Name the parasite shown.
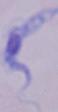

This is a trypanosome.

magnification: 1000x
modality: photomicrograph